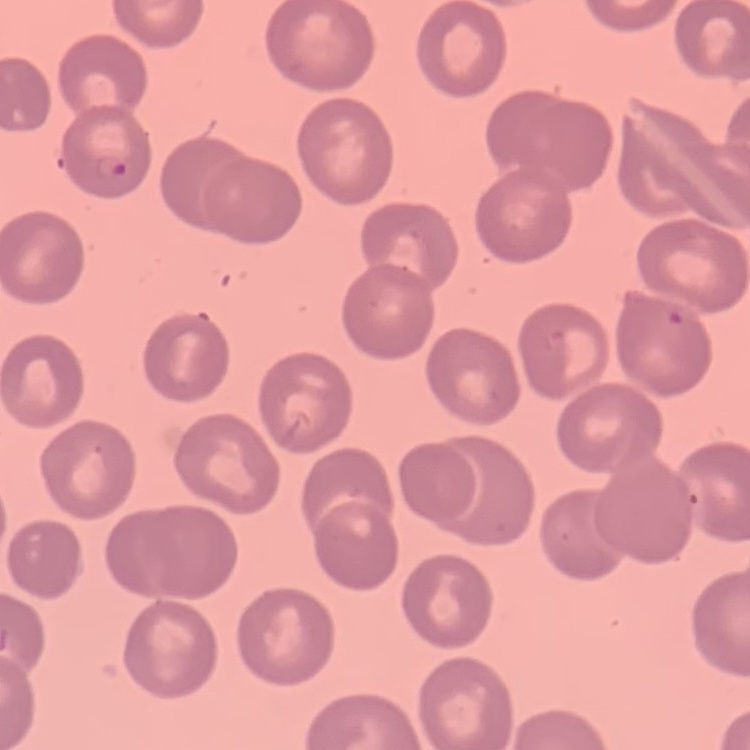
erythrocyte morphology = no rouleaux formation
stain = Field's or Giemsa
preparation = thin blood smear
image type = square crop of a larger photomicrograph